Classify this cell by malaria status.
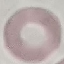

It is uninfected.

preparation = thin smear
capture = smartphone through the microscope eyepiece
stain = Giemsa
image type = automatically extracted cell patch, resized to 64 × 64 pixels